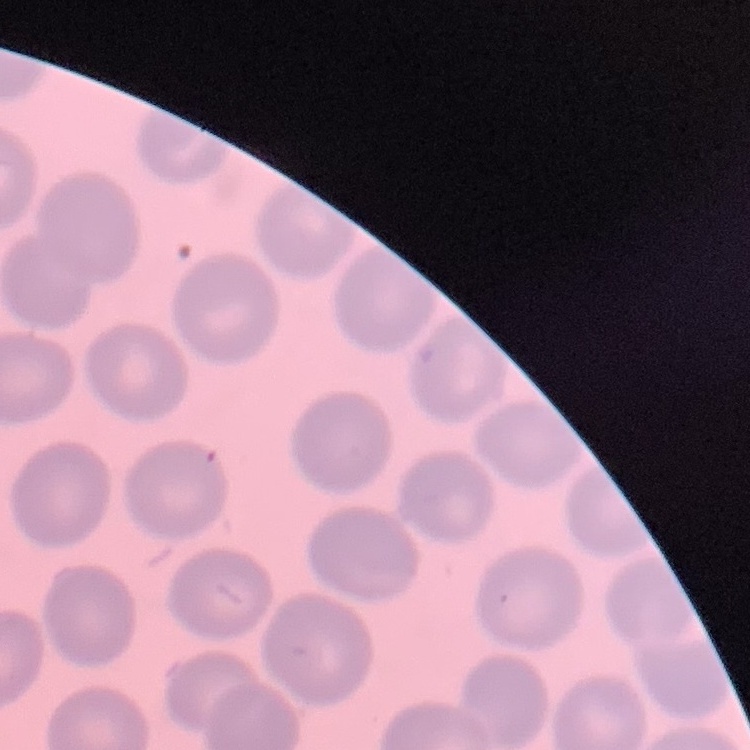

The red blood cells exhibit no rouleaux formation. Stained with either Field's or Giemsa. Thin peripheral smear. Square crop of a larger photomicrograph.